Identify the parasite.
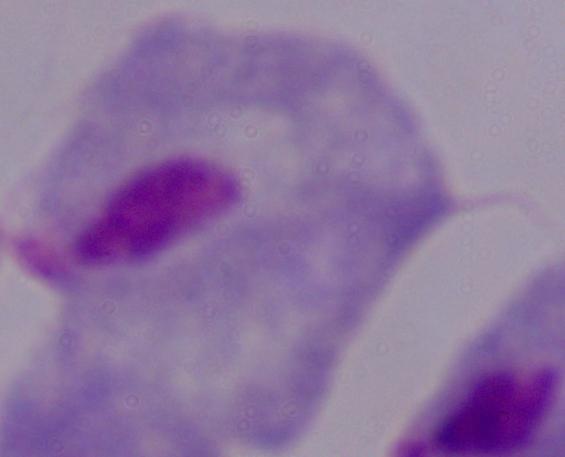
A trichomonad.

Summary:
  - Modality: micrograph
  - Magnification: 1000x